Identify the blood parasite species.
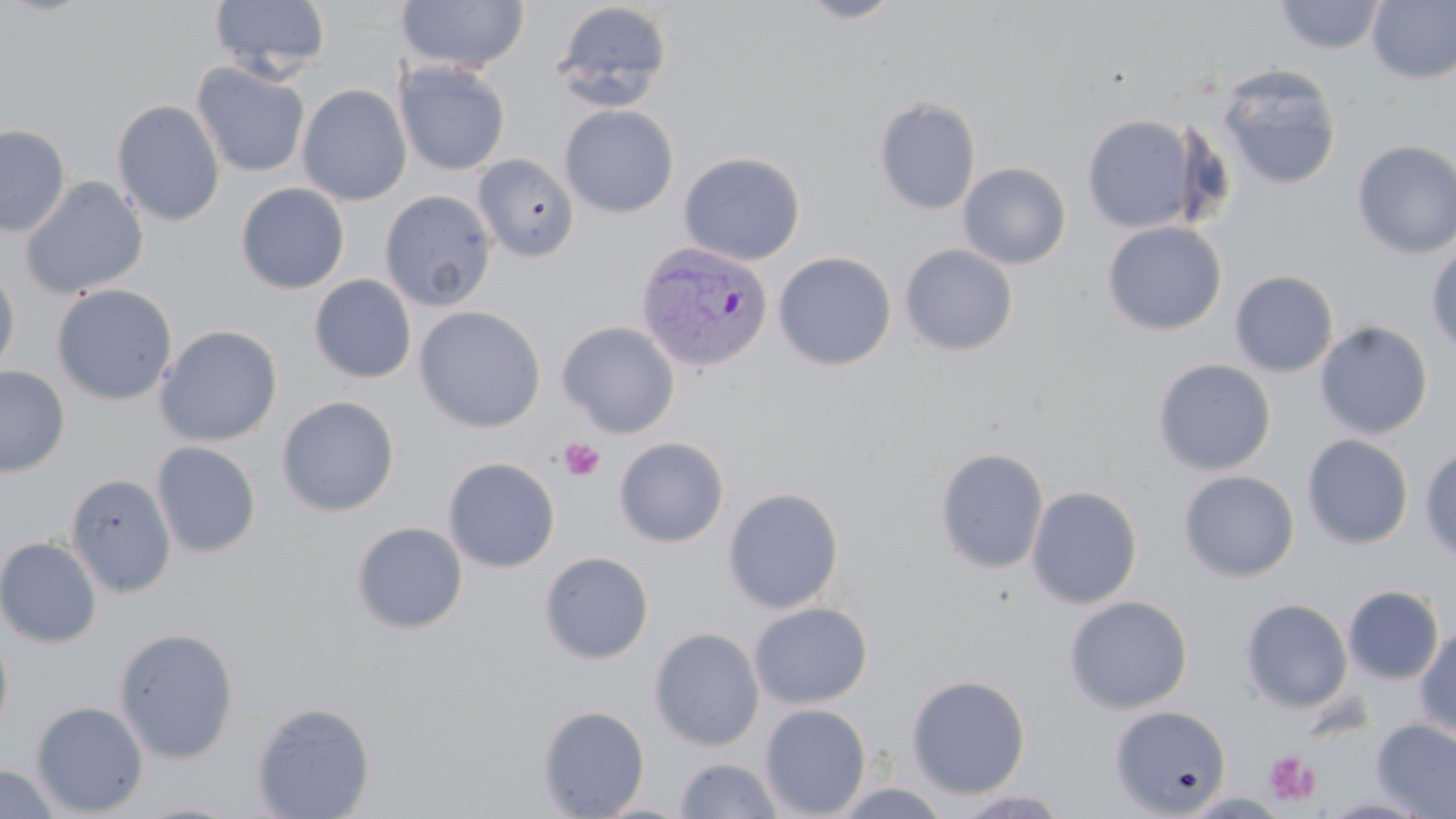
Plasmodium vivax.

Summary:
  - Coordinate format: approximate bounding boxes as (x1,y1)-(x2,y2) corner pairs in pixels
  - Platelet locations: (559,438)-(606,481), (1263,751)-(1322,807)
  - Uninfected red blood cell locations: (209,0)-(332,81), (396,0)-(529,73), (795,0)-(905,24), (1273,0)-(1387,55), (1367,1)-(1456,84), (551,2)-(673,112), (191,61)-(311,178), (395,61)-(510,175), (1215,63)-(1342,190), (297,84)-(411,206), (873,97)-(981,215), (112,100)-(225,227), (559,104)-(679,218), (1082,114)-(1200,233), (0,124)-(70,237), (1351,140)-(1456,259), (679,151)-(806,266), (473,154)-(579,262), (958,163)-(1071,269), (20,176)-(149,299), (236,183)-(350,294), (379,190)-(497,312), (1102,221)-(1227,335), (1426,243)-(1456,356), (899,244)-(1018,356), (773,251)-(896,371), (0,262)-(20,380), (1229,270)-(1338,377), (309,275)-(416,383), (53,284)-(177,405), (414,306)-(546,433), (557,321)-(679,438), (1314,321)-(1433,439), (155,324)-(282,447), (1152,358)-(1276,475), (0,365)-(70,477), (277,396)-(399,517), (1301,434)-(1414,549), (613,437)-(729,547), (151,442)-(261,558), (1419,446)-(1456,563), (934,447)-(1049,574), (443,457)-(560,573), (1177,470)-(1300,582), (66,473)-(177,597), (1026,485)-(1142,609), (723,487)-(844,614), (351,522)-(468,634), (0,537)-(102,648), (539,551)-(654,664), (1343,585)-(1444,684), (1064,595)-(1193,714), (1240,599)-(1353,713), (748,602)-(873,709), (0,626)-(14,741), (1414,626)-(1456,741), (114,627)-(239,764), (649,627)-(765,751), (905,674)-(1030,798), (30,701)-(148,817), (251,702)-(376,818), (760,703)-(872,818), (1110,704)-(1232,817), (537,705)-(650,818), (1371,719)-(1456,818), (673,757)-(784,818), (0,763)-(62,819), (829,783)-(955,818), (952,789)-(1072,818), (1318,795)-(1436,818)
  - Plasmodium vivax-infected red blood cell locations: (634,240)-(772,373)
  - Field of view: single
  - Magnification: 1000x
  - Image size: 1456×819 pixels
  - Preparation: thin blood film
  - Stain: May-Grünwald-Giemsa
  - Modality: optical microscopy